Report the malaria status of this cell.
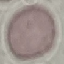
It is uninfected.

Summary:
  - Image type: automatically extracted cell patch, resized to 64 × 64 pixels
  - Stain: Giemsa
  - Preparation: thin blood film
  - Capture: smartphone camera at the microscope eyepiece